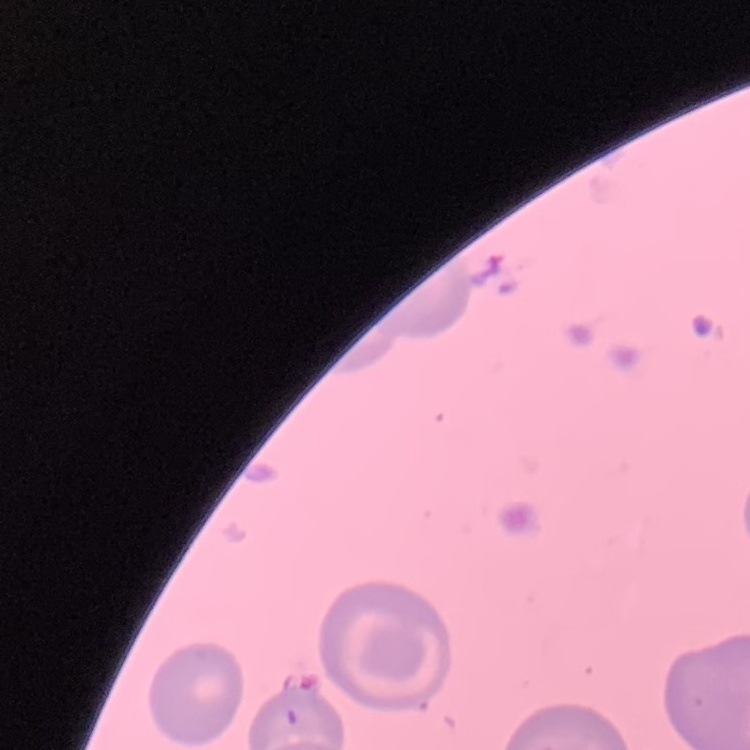

erythrocyte_morphology: no rouleaux formation
preparation: thin peripheral smear
image_type: square crop of a larger photomicrograph
stain: Field's or Giemsa